State which parasite is depicted.
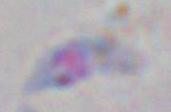

Toxoplasma gondii.

Summary:
  - Magnification: 1000x
  - Modality: micrograph